Describe the morphology of the red blood cells.
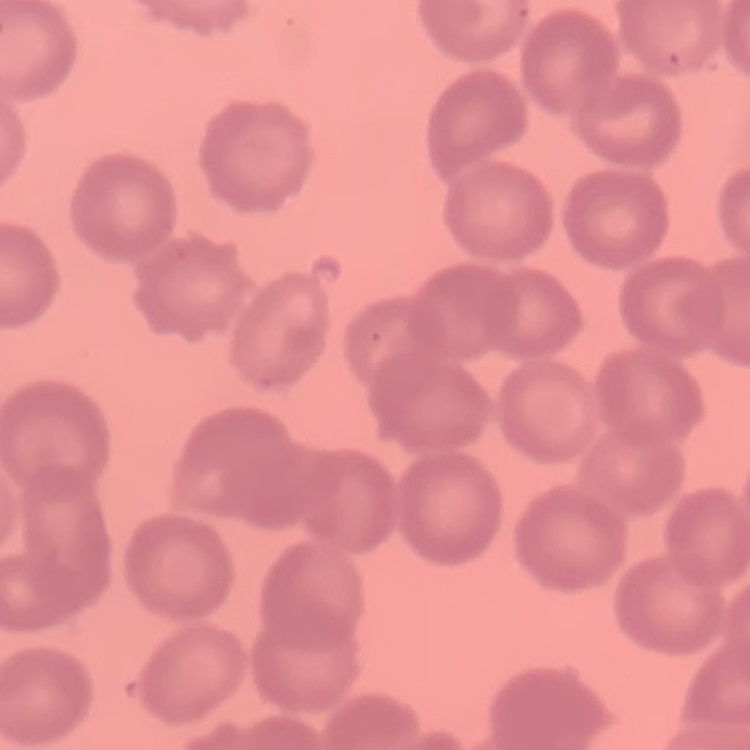

No rouleaux formation.

Summary:
  - Stain: Field's or Giemsa
  - Preparation: thin blood film
  - Image type: one tile cut from a larger photomicrograph